Point out each leukocyte.
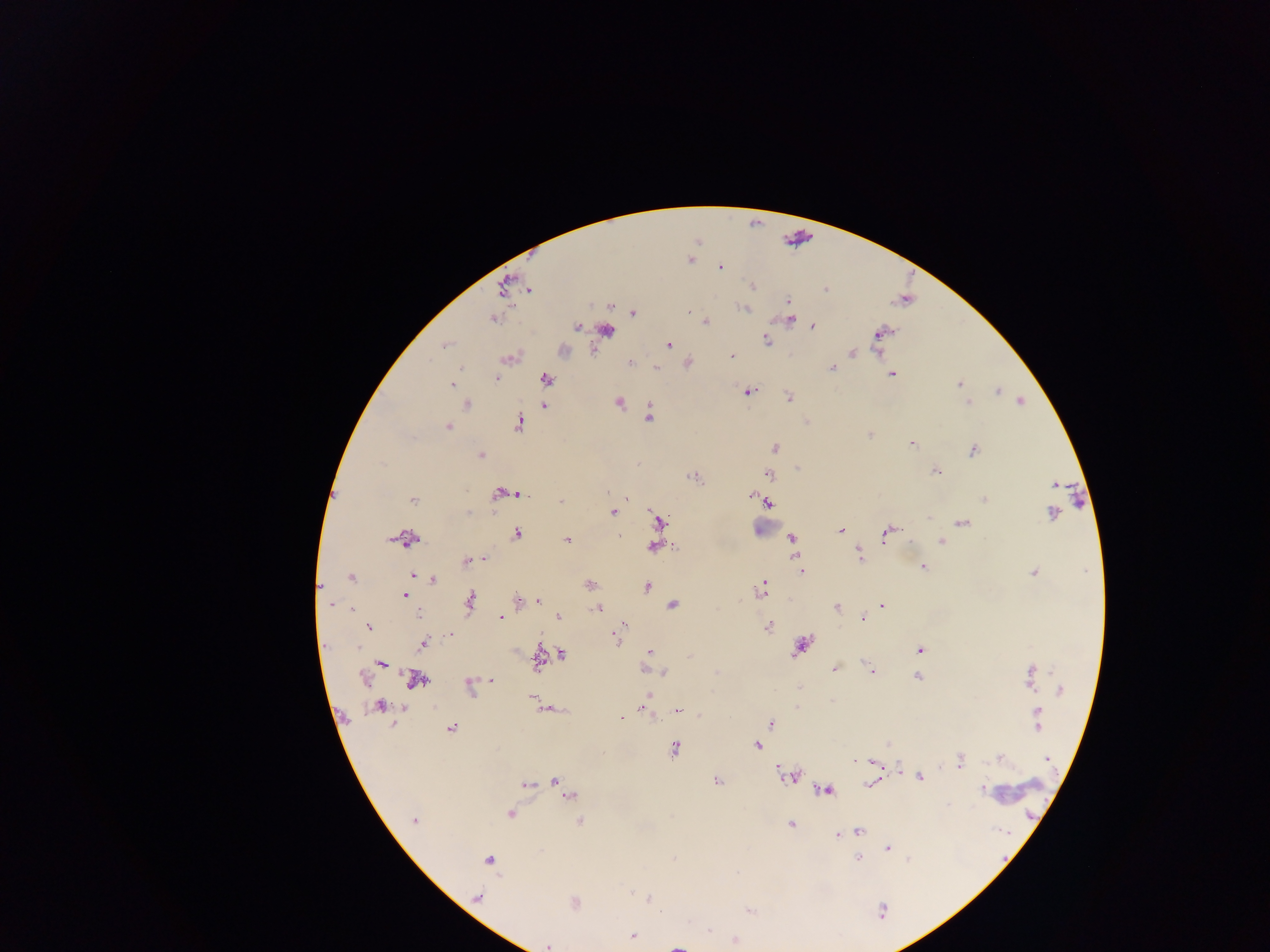

Approximate centers as x y in pixels.
Leukocytes: 766 525.

Malaria parasite locations: 691 259; 719 266; 752 285; 504 286; 529 289; 825 290; 787 302; 610 305; 746 308; 688 311; 632 313; 492 318; 788 319; 705 322; 812 326; 576 327; 606 330; 880 333; 766 340; 445 343; 668 345; 562 351; 853 352; 731 356; 507 357; 630 362; 686 363; 655 368; 832 368; 891 374; 495 377; 545 379; 452 383; 959 384; 748 391; 996 391; 788 397; 1021 401; 618 402; 967 402; 467 403; 543 406; 648 415; 517 423; 447 426; 870 434; 911 443; 774 448; 972 450; 479 455; 797 468; 935 470; 769 474; 693 476; 1054 484; 499 493; 513 493; 519 494; 749 494; 984 499; 413 500; 560 501; 766 502; 612 512; 1051 513; 656 522; 962 523; 840 530; 887 532; 516 533; 656 534; 619 536; 791 537; 405 538; 566 540; 941 540; 654 545; 859 555; 478 559; 485 559; 797 559; 467 560; 922 566; 801 571; 1034 572; 351 577; 432 580; 588 584; 319 586; 646 586; 761 590; 405 595; 538 600; 469 601; 519 601; 330 604; 672 604; 882 605; 836 607; 351 608; 597 608; 558 616; 501 617; 861 619; 768 625; 368 626; 449 633; 617 639; 423 643; 801 645; 919 650; 649 652; 561 654; 538 657; 382 663; 835 668; 646 670; 663 671; 871 671; 916 676; 1029 676; 364 678; 490 679; 415 680; 469 687; 1060 689; 647 694; 532 697; 644 703; 380 705; 548 708; 677 709; 1038 712; 620 717; 770 724; 1036 725; 451 728; 756 745; 674 748; 1000 758; 1046 758; 854 760; 959 760; 876 764; 897 771; 919 776; 788 777; 717 780; 554 781; 872 783; 524 785; 981 788; 825 789; 569 796; 511 813; 414 820; 580 821; 790 824; 858 831; 836 835; 887 848; 857 858; 488 859; 477 897; 647 899; 574 903; 881 910; 749 911; 708 930; 632 935; 734 941; 548 945; 677 945. Photographed through a microscope with a mobile-phone camera. Image is 1270×952 pixels. Thick blood smear. Collected in Ghana. Single field of view.